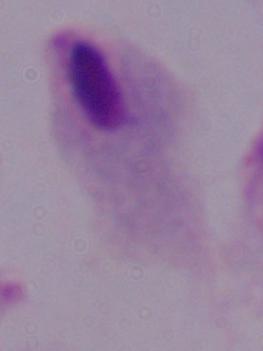 A trichomonad is shown. Micrograph. Captured at 1000x magnification.